Classify this cell by malaria status.
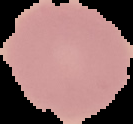

It is uninfected.

Summary:
  - Image type: segmented cell region on a black background
  - Image size: 133×124 pixels
  - Preparation: thin blood film